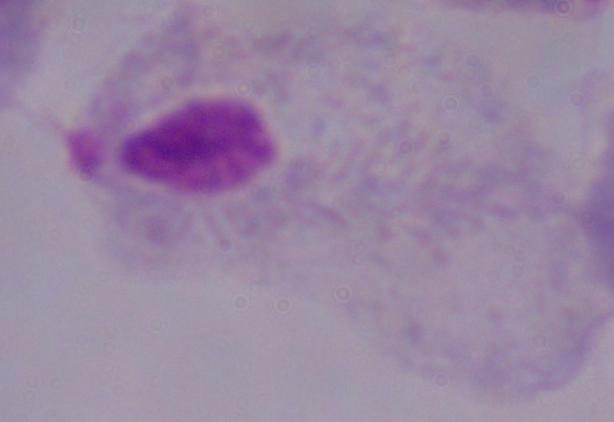
Summary:
  - Magnification: 1000x
  - Identification: trichomonad
  - Modality: micrograph